Mark where platelets are.
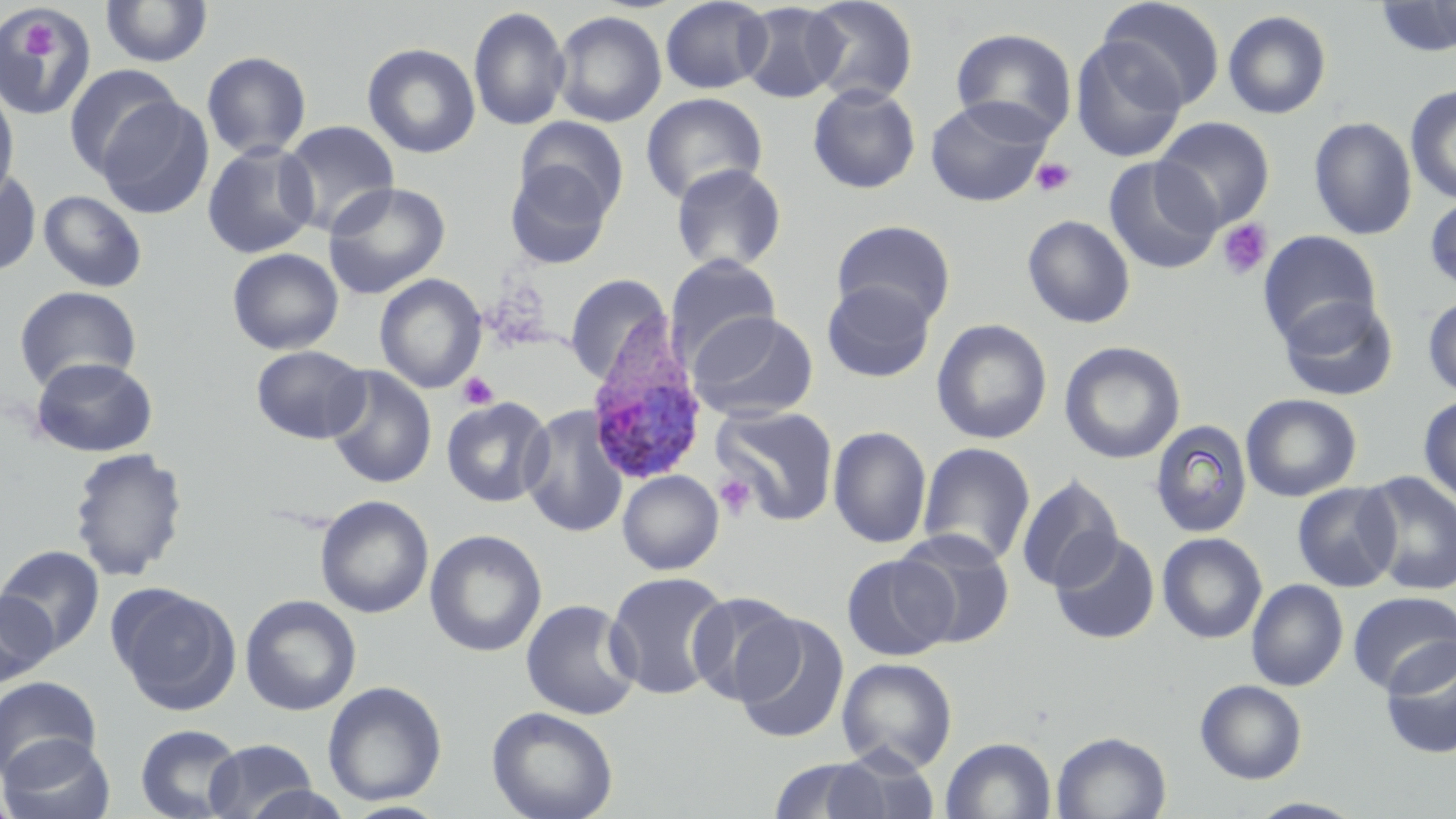
Approximate bounding boxes as (x1,y1)-(x2,y2) corner pairs in pixels.
Platelets: (19,24)-(58,60), (1031,157)-(1075,197), (1217,219)-(1273,280), (458,372)-(498,410), (714,474)-(755,518).

Summary:
  - Uninfected red blood cell locations: (100,0)-(213,68), (660,0)-(772,94), (803,0)-(919,105), (1099,0)-(1226,110), (1374,0)-(1456,58), (737,2)-(846,104), (0,6)-(98,119), (468,6)-(571,132), (551,9)-(667,127), (1222,10)-(1332,119), (950,27)-(1078,142), (1069,35)-(1187,163), (362,42)-(481,158), (201,51)-(312,160), (62,64)-(183,181), (0,83)-(19,207), (808,83)-(921,194), (1405,84)-(1456,204), (640,92)-(767,205), (925,95)-(1054,207), (96,96)-(214,218), (515,116)-(629,220), (1154,116)-(1275,230), (1309,116)-(1417,240), (279,120)-(400,237), (202,140)-(319,259), (1103,156)-(1222,274), (504,161)-(615,268), (670,163)-(787,273), (0,168)-(42,277), (322,182)-(451,299), (38,190)-(147,292), (1424,195)-(1456,293), (1022,215)-(1136,328), (832,220)-(956,326), (1257,231)-(1383,347), (227,247)-(344,355), (664,253)-(781,367), (374,273)-(487,394), (564,274)-(672,385), (822,279)-(936,383), (14,285)-(142,392), (1422,294)-(1456,398), (1276,295)-(1399,401), (689,311)-(818,422), (931,319)-(1052,445), (931,326)-(1186,449), (1059,341)-(1186,464), (251,344)-(369,444), (30,356)-(158,457), (324,366)-(437,489), (1241,393)-(1362,502), (1418,394)-(1456,509), (441,396)-(554,508), (520,403)-(629,539), (712,405)-(839,525), (1149,418)-(1253,538), (827,426)-(932,548), (917,442)-(1036,565), (68,446)-(189,582), (617,470)-(724,575), (1358,471)-(1456,596), (1015,475)-(1124,592), (1292,482)-(1400,591), (314,495)-(434,619), (425,529)-(548,657), (895,529)-(1016,649), (1157,532)-(1268,643), (1050,533)-(1161,645), (0,545)-(104,656), (841,554)-(957,660), (605,571)-(732,700), (1246,579)-(1348,691), (111,584)-(240,714), (0,589)-(56,686), (686,590)-(802,706), (1347,590)-(1456,695), (240,594)-(361,716), (520,598)-(642,720), (732,612)-(850,745), (1379,640)-(1456,760), (836,657)-(958,773), (0,676)-(102,779), (1194,679)-(1308,784), (322,680)-(447,806), (486,706)-(619,819), (135,724)-(245,818), (1051,730)-(1172,819), (0,733)-(116,819), (941,736)-(1057,819), (203,739)-(318,818), (765,756)-(894,819), (240,785)-(357,819), (1247,798)-(1367,818)
  - Plasmodium ovale-infected red blood cell locations: (584,322)-(709,487)
  - Slide-level diagnosis: Plasmodium ovale
  - Modality: optical microscopy
  - Preparation: thin blood smear
  - Field of view: single
  - Stain: May-Grünwald-Giemsa
  - Image size: 1456×819 pixels
  - Magnification: 1000x